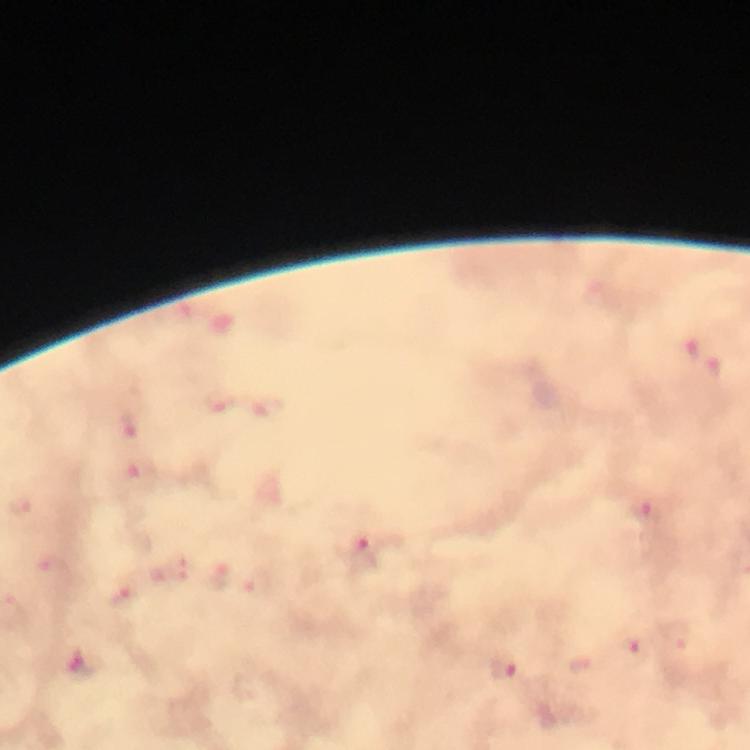
magnification: 100x
immersion_oil: applied
capture: smartphone mounted on the microscope
malaria_parasite_locations: 'approximate object centers, in pixels from the top-left corner: (x=695, y=346), (x=219, y=401), (x=129, y=427), (x=19, y=506), (x=654, y=511), (x=362, y=547), (x=54, y=572), (x=120, y=597), (x=631, y=650), (x=505, y=669)'
cropped_from: a single field of view
stain: Giemsa
preparation: thick blood film
context: from a malaria diagnostic workup
image_size: 750×750 pixels